Evaluate for Plasmodium parasites.
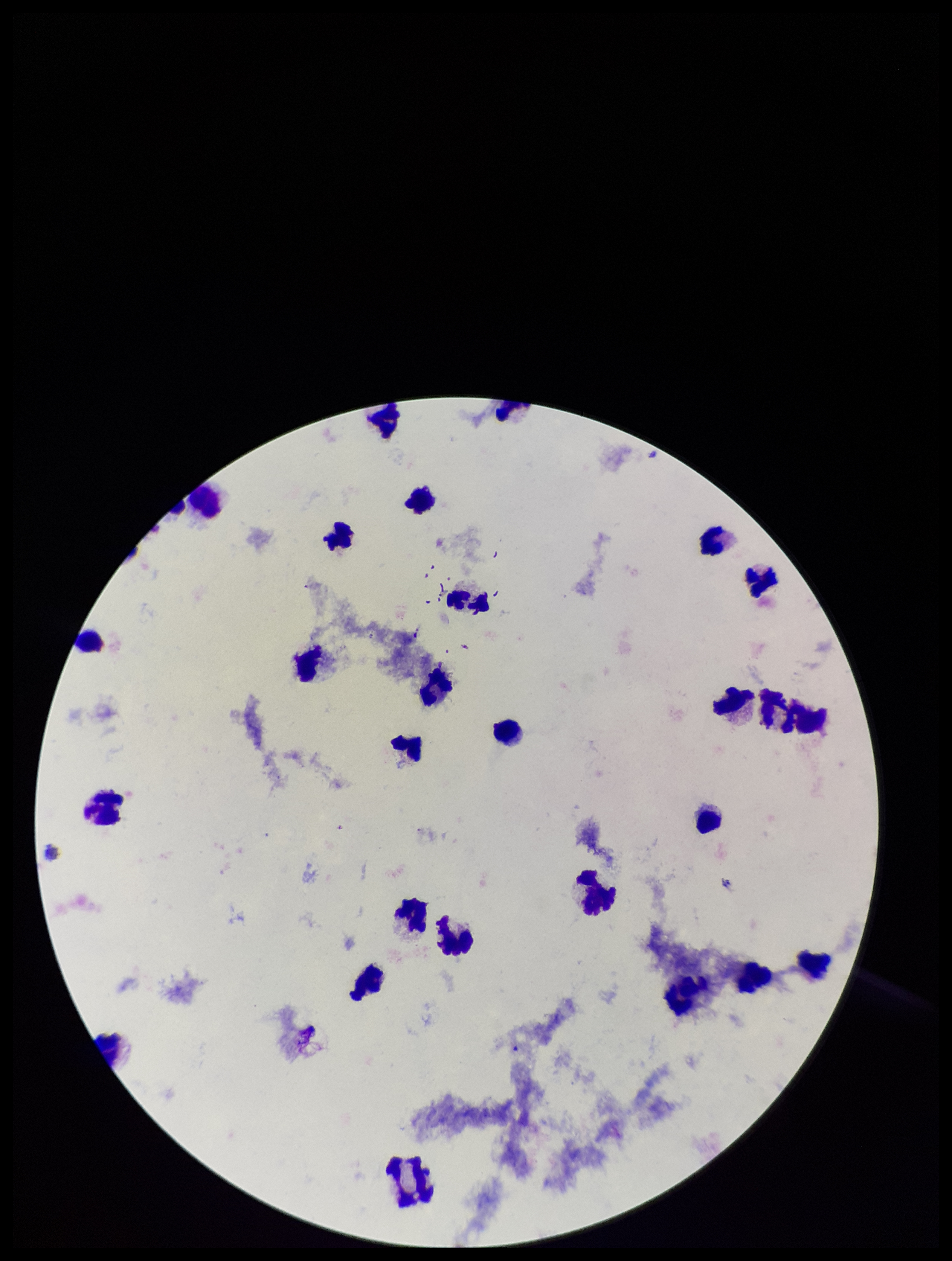
None identified.

Giemsa stain. Patient malaria status: negative. Photographed through the microscope eyepiece with a smartphone camera. Parasite count: 0. Leukocyte count: 27. Image is 952×1261 pixels. Preparation: thick. One field from this slide.